State the blood parasite species.
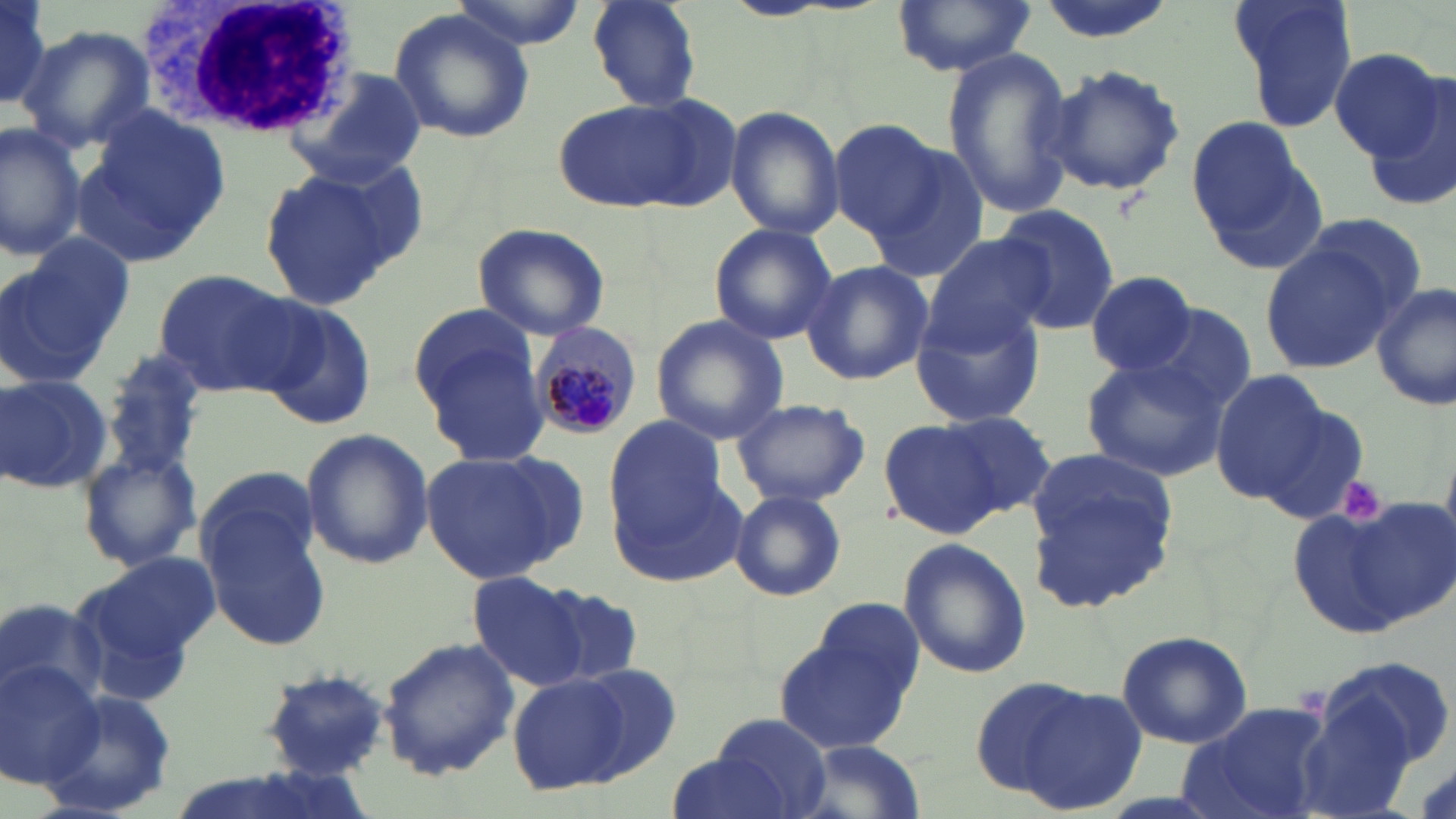
Plasmodium malariae.

Approximate bounding boxes as (x1,y1)-(x2,y2) corner pairs in pixels. White blood cell locations: (145,0)-(359,143). Plasmodium malariae-infected red blood cell locations: (526,319)-(646,444). Uninfected red blood cell locations: (0,0)-(61,116), (448,0)-(592,53), (1227,0)-(1357,130), (586,1)-(702,112), (891,1)-(1036,77), (389,6)-(536,146), (15,24)-(153,152), (940,49)-(1076,219), (1325,49)-(1444,163), (1044,63)-(1187,199), (295,71)-(428,182), (1360,76)-(1456,212), (554,97)-(720,214), (76,104)-(234,265), (725,105)-(845,241), (1186,113)-(1325,262), (828,120)-(949,239), (0,122)-(84,261), (864,144)-(990,283), (258,166)-(405,309), (991,203)-(1120,333), (1302,214)-(1427,317), (472,221)-(611,341), (708,223)-(838,347), (924,232)-(1058,348), (6,235)-(135,382), (1259,242)-(1397,373), (800,259)-(932,386), (151,267)-(300,395), (1085,270)-(1200,376), (1372,281)-(1455,412), (908,295)-(1047,428), (253,301)-(380,430), (408,302)-(541,421), (1136,305)-(1257,419), (650,316)-(788,444), (418,338)-(550,467), (101,352)-(208,483), (1082,356)-(1228,481), (1209,369)-(1329,503), (1,372)-(114,496), (1245,388)-(1368,517), (729,396)-(871,508), (939,410)-(1060,518), (878,418)-(1003,538), (604,421)-(738,576), (300,429)-(435,568), (76,444)-(202,575), (418,448)-(581,584), (1023,451)-(1179,614), (194,474)-(333,652), (727,489)-(848,603), (1346,496)-(1455,624), (1289,507)-(1410,638), (898,536)-(1031,680), (73,555)-(218,691), (466,572)-(591,689), (543,588)-(641,685), (802,599)-(928,719), (773,630)-(916,753), (1116,630)-(1253,750), (379,637)-(519,779), (1317,654)-(1453,780), (0,658)-(102,789), (570,662)-(683,781), (259,668)-(394,781), (508,672)-(632,793), (1008,682)-(1150,815), (39,685)-(178,815), (1181,697)-(1336,819), (712,713)-(832,817), (792,740)-(931,819), (662,750)-(798,819). Platelet locations: (1333,473)-(1389,526). One field of a larger specimen. 1000x magnification. Thin blood smear. Image is 1456×819 pixels. Light microscopy. May-Grünwald-Giemsa-stained preparation.